Comment on the morphology of the red blood cells.
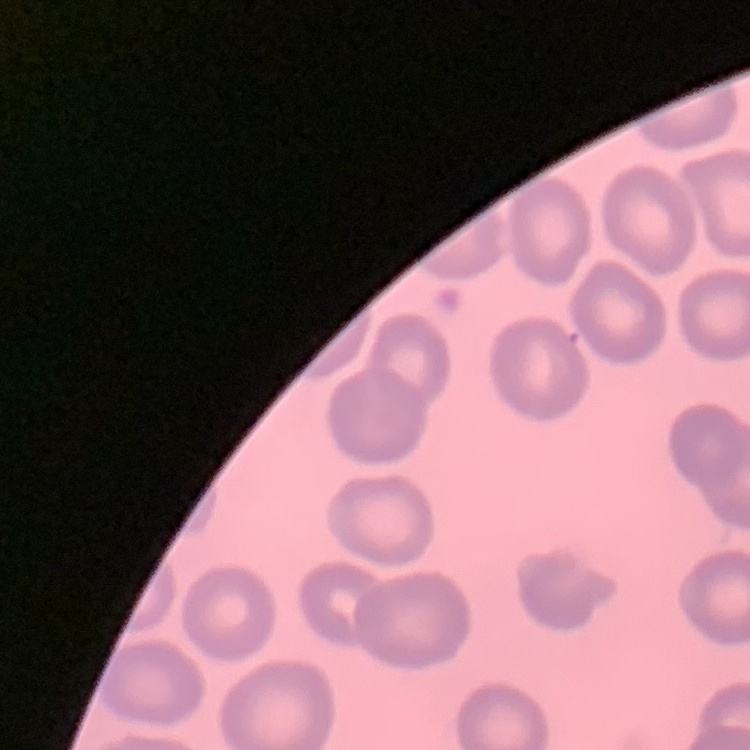
They show no rouleaux formation.

Summary:
  - Image type: one tile cut from a larger photomicrograph
  - Stain: Field's or Giemsa
  - Preparation: thin blood film